Classify this cell by malaria status.
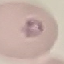

Parasitized.

{
  "image_type": "cell patch, automatically extracted from a larger field of view and resized to 64 × 64 pixels",
  "stain": "Giemsa",
  "capture": "smartphone through the microscope eyepiece",
  "preparation": "thin blood smear"
}